Locate every malaria parasite and every leukocyte.
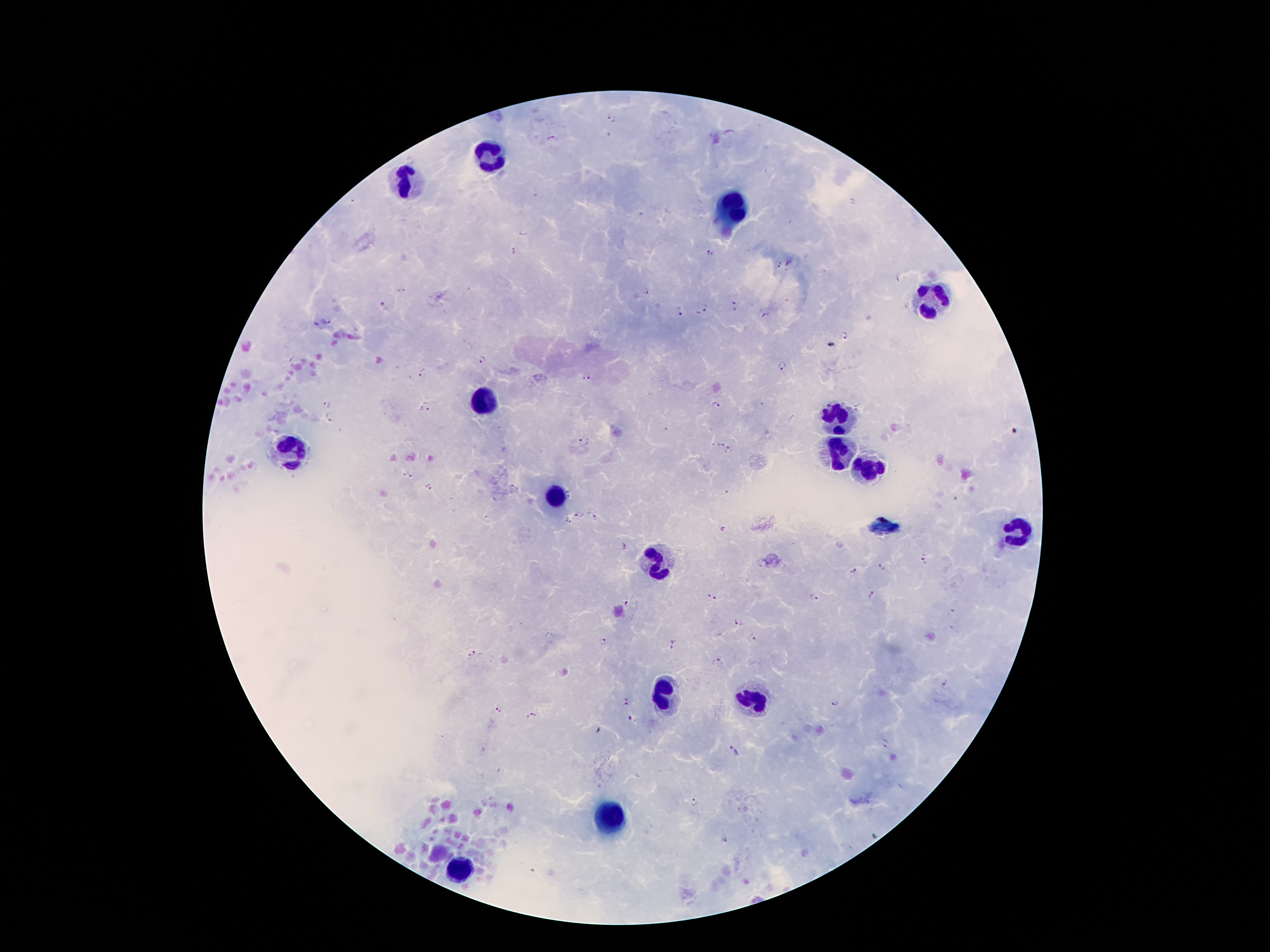

Approximate centers as {x, y} in pixels.
Malaria parasites: {611, 119}, {729, 132}, {550, 138}, {522, 231}, {515, 250}, {709, 253}, {779, 265}, {401, 291}, {645, 292}, {734, 302}, {383, 305}, {706, 308}, {681, 311}, {765, 316}, {329, 320}, {316, 325}, {844, 338}, {480, 359}, {782, 365}, {423, 374}, {587, 377}, {715, 404}, {327, 405}, {425, 406}, {329, 419}, {664, 430}, {584, 441}, {719, 444}, {729, 451}, {406, 475}, {514, 487}, {428, 488}, {570, 494}, {580, 515}, {593, 517}, {567, 520}, {722, 529}, {624, 548}, {923, 560}, {883, 566}, {854, 570}, {871, 595}, {712, 597}, {814, 597}, {629, 604}, {953, 611}, {738, 623}, {754, 636}, {603, 641}, {677, 642}, {472, 652}, {718, 662}, {944, 682}, {627, 702}, {834, 703}, {499, 708}, {531, 716}, {630, 718}, {886, 744}, {735, 750}, {694, 803}, {725, 840}.
Leukocytes: {492, 156}, {410, 178}, {731, 210}, {938, 301}, {483, 400}, {838, 415}, {287, 449}, {838, 451}, {869, 464}, {554, 497}, {1017, 531}, {653, 559}, {664, 695}, {752, 701}, {610, 819}, {457, 871}.

Summary:
  - Patient malaria status: infected with Plasmodium falciparum
  - Preparation: thick peripheral-blood smear
  - Field of view: single
  - Capture: smartphone through the microscope eyepiece
  - Stain: Giemsa
  - Magnification: 100x
  - Image size: 1270×952 pixels